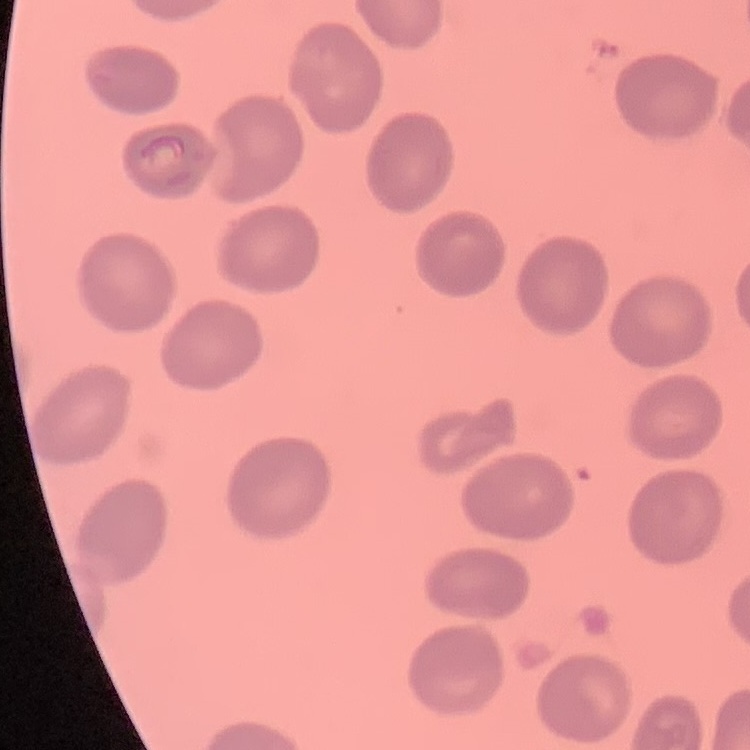

The red blood cells show no rouleaux formation. Stained with either Field's or Giemsa. Thin blood film. Square crop of a larger photomicrograph.